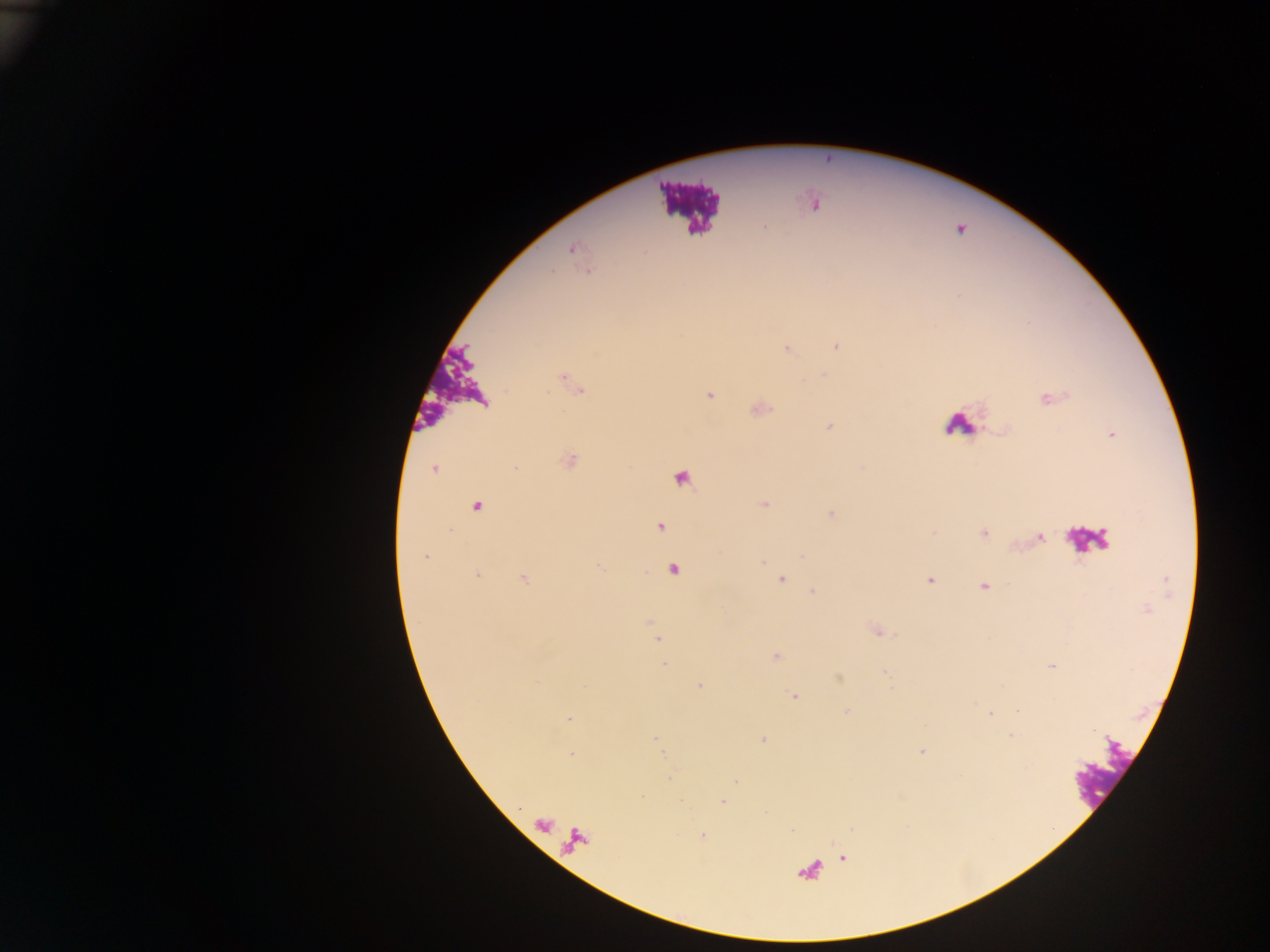

Approximate centers as {x, y} in pixels. Leukocyte locations: {682, 206}, {955, 428}, {1103, 772}. Plasmodium parasite locations: {815, 205}, {765, 226}, {961, 230}, {570, 249}, {835, 344}, {822, 374}, {709, 395}, {1046, 399}, {829, 425}, {433, 468}, {764, 502}, {831, 513}, {982, 533}, {1039, 537}, {801, 557}, {424, 558}, {765, 560}, {599, 567}, {481, 573}, {524, 578}, {782, 579}, {929, 580}, {813, 590}, {877, 631}, {659, 640}, {774, 657}, {663, 664}, {1051, 665}, {700, 687}, {797, 695}, {1018, 711}, {989, 714}, {568, 719}, {1012, 734}, {764, 739}, {657, 743}, {923, 751}, {572, 755}, {672, 777}, {735, 781}, {642, 797}, {680, 801}, {723, 802}, {765, 813}, {790, 830}, {703, 835}, {845, 857}. Photographed through a microscope with a mobile-phone camera. Thick blood film. Single field of view. Sample from Ghana. Image is 1270×952 pixels.